Identify the parasite.
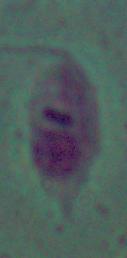
This is Leishmania.

Photomicrograph. 1000x magnification.